Comment on the morphology of the erythrocytes.
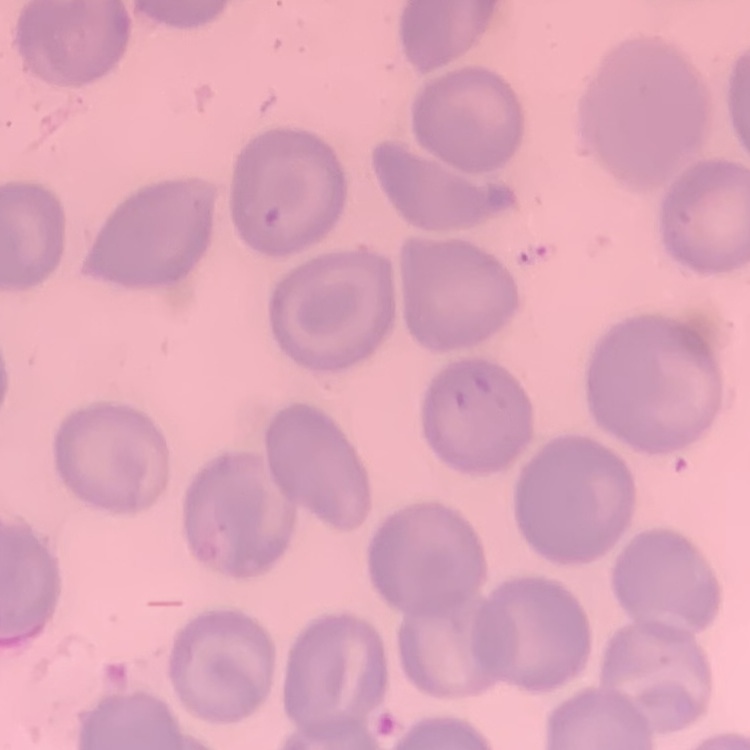

They show no rouleaux formation.

{
  "preparation": "thin blood smear",
  "stain": "Field's or Giemsa",
  "image_type": "one tile cut from a larger photomicrograph"
}